Identify the blood parasite species.
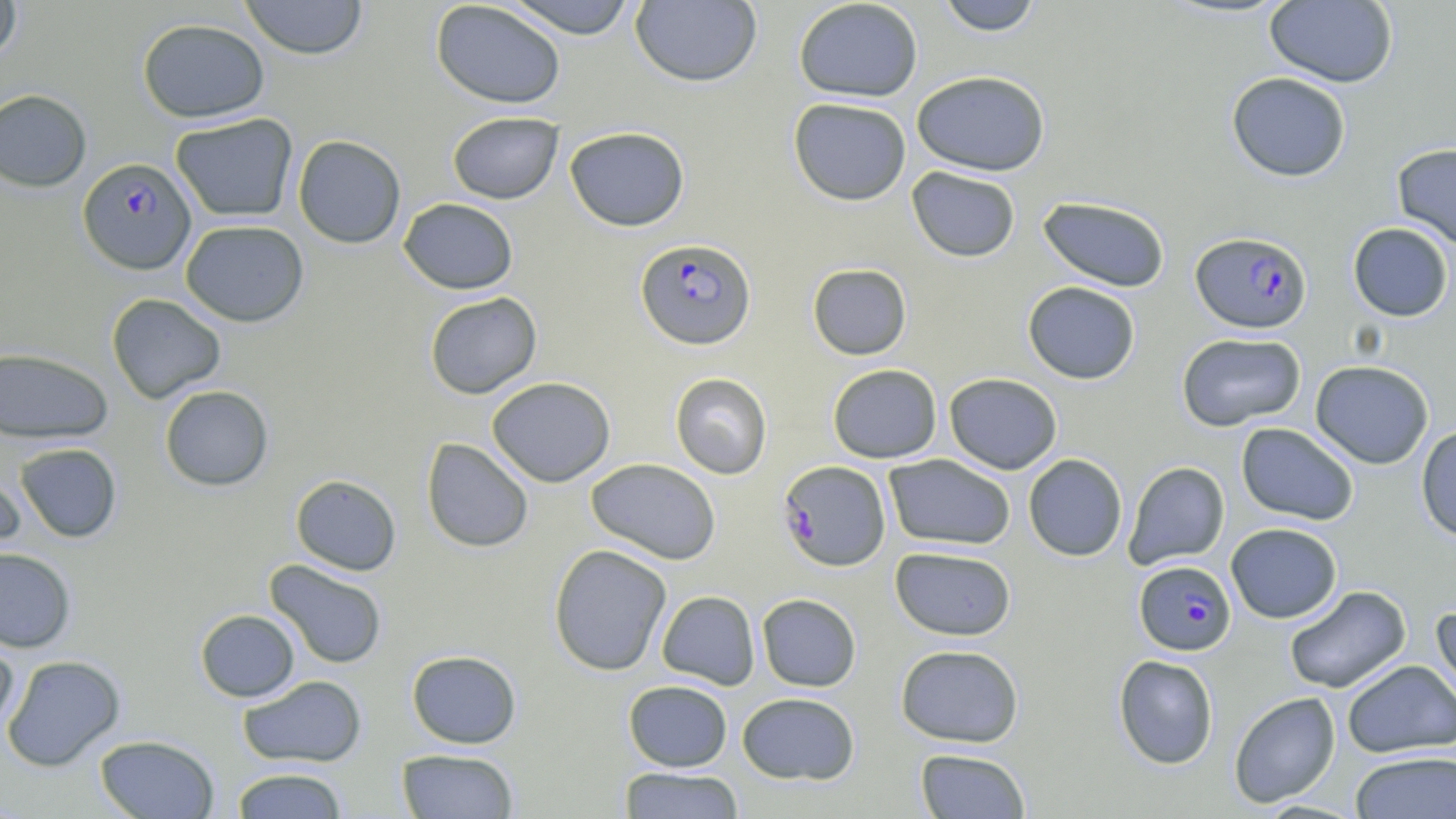
Plasmodium falciparum.

Approximate bounding boxes as (x1, y1, x2, y2) in pixels. Plasmodium falciparum-infected red blood cell locations: (78, 157, 196, 275), (1191, 231, 1312, 334), (635, 237, 756, 350), (777, 460, 891, 571), (1134, 560, 1236, 655). Uninfected red blood cell locations: (0, 0, 22, 64), (239, 0, 369, 60), (503, 0, 639, 39), (792, 0, 923, 102), (936, 0, 1044, 35), (1264, 0, 1398, 88), (430, 1, 566, 109), (630, 1, 762, 88), (137, 18, 270, 123), (911, 70, 1050, 176), (1226, 72, 1351, 182), (0, 89, 92, 192), (788, 97, 912, 206), (447, 111, 563, 204), (170, 113, 298, 222), (564, 126, 690, 231), (292, 134, 406, 249), (1392, 142, 1456, 249), (907, 166, 1021, 262), (1037, 196, 1171, 293), (399, 197, 519, 294), (180, 219, 309, 327), (1347, 222, 1454, 322), (807, 263, 912, 360), (1023, 281, 1140, 385), (424, 292, 542, 399), (106, 293, 226, 404), (1176, 332, 1306, 432), (0, 346, 114, 443), (1310, 360, 1434, 469), (827, 363, 942, 463), (670, 372, 773, 479), (944, 372, 1063, 474), (487, 377, 615, 487), (159, 385, 274, 491), (1235, 422, 1359, 525), (1415, 425, 1456, 543), (421, 437, 534, 553), (15, 443, 122, 543), (884, 454, 1016, 551), (1023, 454, 1128, 561), (586, 458, 721, 564), (1123, 461, 1230, 570), (0, 465, 26, 560), (290, 474, 401, 576), (1226, 522, 1342, 623), (548, 544, 672, 676), (0, 546, 77, 653), (889, 546, 1016, 641), (264, 559, 388, 670), (1284, 585, 1411, 694), (656, 590, 760, 689), (756, 593, 862, 691), (1430, 604, 1456, 714), (195, 609, 300, 702), (0, 632, 19, 741), (895, 644, 1024, 747), (406, 650, 522, 749), (2, 654, 125, 772), (1113, 654, 1219, 769), (1342, 659, 1456, 758), (237, 675, 368, 768), (623, 680, 733, 771), (1228, 691, 1341, 807), (737, 692, 860, 785), (94, 734, 219, 818), (396, 748, 519, 818), (915, 748, 1031, 818), (1350, 751, 1456, 819), (619, 767, 744, 818), (231, 768, 348, 818). Optical microscopy. Image is 1456×819 pixels. One field of a larger specimen. Thin blood smear. 1000x magnification. May-Grünwald-Giemsa stain.